Locate and identify every blood parasite.
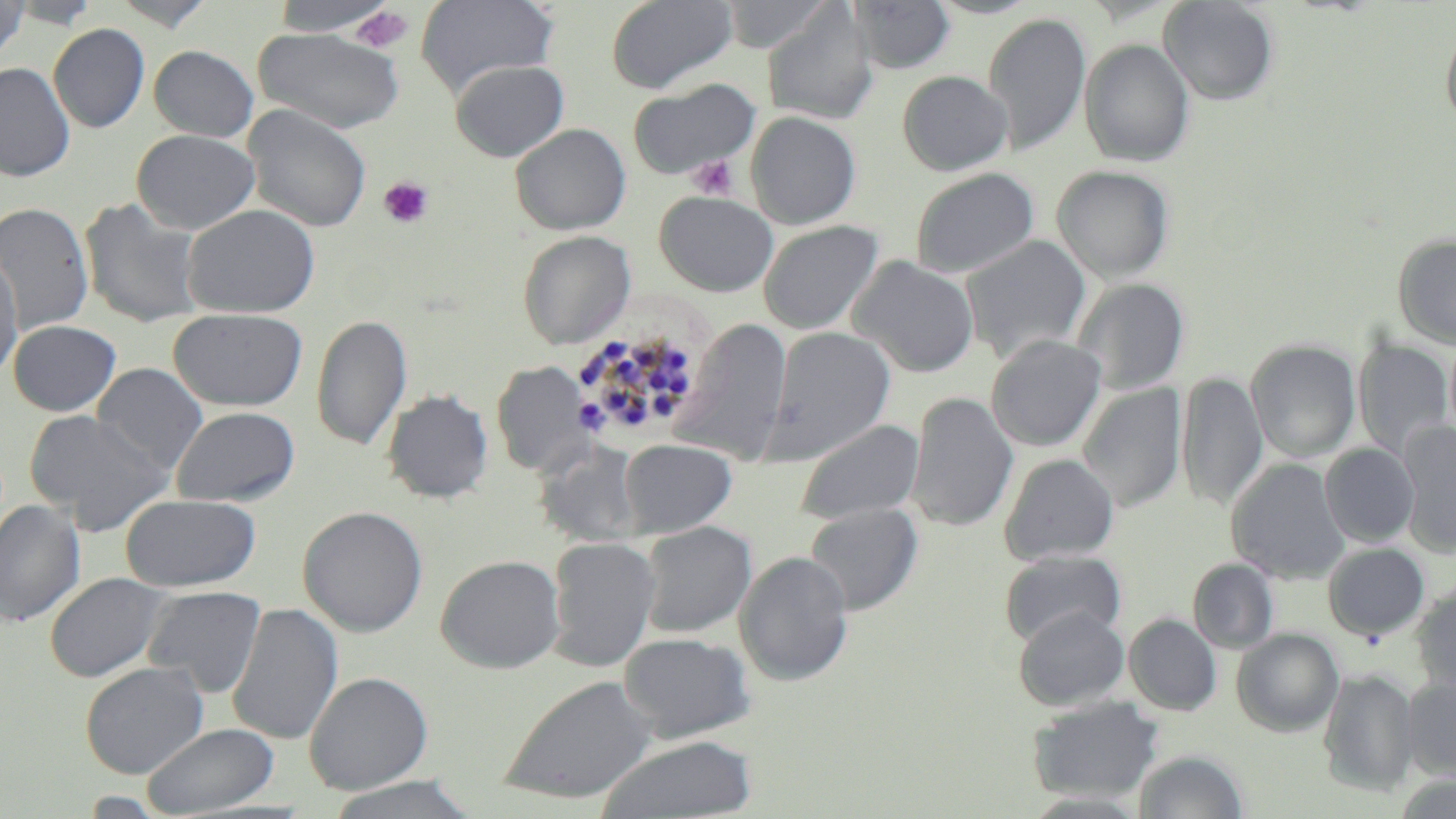
Approximate bounding boxes as named x1/y1/x2/y2 corners in pixels.
Plasmodium malariae-infected red blood cells: (x1=567, y1=328, x2=692, y2=438).
No Plasmodium falciparum, Plasmodium ovale, Plasmodium vivax, Babesia divergens, or Trypanosoma brucei observed.

Summary:
  - Uninfected red blood cell locations: (x1=0, y1=0, x2=32, y2=61), (x1=10, y1=0, x2=102, y2=29), (x1=108, y1=0, x2=216, y2=30), (x1=266, y1=0, x2=404, y2=36), (x1=415, y1=0, x2=558, y2=97), (x1=606, y1=0, x2=737, y2=94), (x1=720, y1=0, x2=834, y2=53), (x1=851, y1=0, x2=955, y2=73), (x1=927, y1=0, x2=1044, y2=19), (x1=1157, y1=0, x2=1279, y2=105), (x1=762, y1=5, x2=879, y2=125), (x1=982, y1=12, x2=1091, y2=156), (x1=48, y1=23, x2=150, y2=133), (x1=1441, y1=24, x2=1456, y2=128), (x1=252, y1=28, x2=404, y2=133), (x1=1079, y1=38, x2=1195, y2=166), (x1=148, y1=45, x2=258, y2=142), (x1=449, y1=59, x2=569, y2=162), (x1=0, y1=62, x2=75, y2=181), (x1=897, y1=70, x2=1012, y2=176), (x1=626, y1=79, x2=759, y2=180), (x1=242, y1=104, x2=372, y2=233), (x1=745, y1=111, x2=861, y2=229), (x1=510, y1=123, x2=631, y2=235), (x1=131, y1=129, x2=260, y2=235), (x1=1052, y1=165, x2=1174, y2=283), (x1=910, y1=167, x2=1039, y2=279), (x1=654, y1=191, x2=779, y2=297), (x1=79, y1=198, x2=206, y2=328), (x1=0, y1=202, x2=94, y2=335), (x1=181, y1=204, x2=320, y2=318), (x1=758, y1=220, x2=883, y2=335), (x1=518, y1=230, x2=635, y2=348), (x1=1392, y1=233, x2=1456, y2=349), (x1=960, y1=235, x2=1091, y2=363), (x1=0, y1=249, x2=24, y2=382), (x1=848, y1=256, x2=979, y2=377), (x1=1074, y1=277, x2=1189, y2=394), (x1=168, y1=307, x2=307, y2=411), (x1=312, y1=314, x2=412, y2=452), (x1=672, y1=318, x2=793, y2=464), (x1=8, y1=319, x2=121, y2=416), (x1=766, y1=325, x2=895, y2=463), (x1=985, y1=334, x2=1106, y2=452), (x1=1352, y1=338, x2=1454, y2=460), (x1=1245, y1=339, x2=1361, y2=463), (x1=492, y1=361, x2=595, y2=477), (x1=92, y1=363, x2=208, y2=476), (x1=1177, y1=372, x2=1268, y2=511), (x1=1077, y1=382, x2=1187, y2=512), (x1=382, y1=389, x2=492, y2=503), (x1=907, y1=392, x2=1018, y2=532), (x1=170, y1=406, x2=300, y2=507), (x1=23, y1=408, x2=173, y2=533), (x1=796, y1=419, x2=924, y2=525), (x1=1397, y1=421, x2=1456, y2=557), (x1=619, y1=439, x2=737, y2=538), (x1=536, y1=441, x2=646, y2=547), (x1=1320, y1=444, x2=1419, y2=546), (x1=999, y1=453, x2=1120, y2=564), (x1=1225, y1=458, x2=1350, y2=584), (x1=120, y1=493, x2=261, y2=592), (x1=0, y1=499, x2=85, y2=626), (x1=804, y1=502, x2=923, y2=616), (x1=297, y1=505, x2=428, y2=637), (x1=638, y1=520, x2=757, y2=637), (x1=546, y1=536, x2=661, y2=672), (x1=1322, y1=542, x2=1429, y2=641), (x1=999, y1=550, x2=1125, y2=648), (x1=734, y1=551, x2=854, y2=686), (x1=436, y1=554, x2=565, y2=673), (x1=1187, y1=558, x2=1278, y2=654), (x1=44, y1=572, x2=170, y2=682), (x1=1411, y1=581, x2=1456, y2=695), (x1=142, y1=585, x2=266, y2=697), (x1=226, y1=602, x2=344, y2=746), (x1=1013, y1=606, x2=1129, y2=710), (x1=1124, y1=614, x2=1222, y2=715), (x1=1231, y1=628, x2=1344, y2=736), (x1=619, y1=631, x2=755, y2=742), (x1=80, y1=662, x2=209, y2=778), (x1=1318, y1=668, x2=1420, y2=796), (x1=303, y1=671, x2=433, y2=794), (x1=499, y1=674, x2=658, y2=805), (x1=1401, y1=677, x2=1456, y2=780), (x1=1026, y1=695, x2=1164, y2=804), (x1=142, y1=722, x2=280, y2=816), (x1=595, y1=735, x2=757, y2=819), (x1=1134, y1=749, x2=1248, y2=818), (x1=324, y1=775, x2=480, y2=819)
  - Platelet locations: (x1=351, y1=6, x2=415, y2=54), (x1=685, y1=155, x2=739, y2=199), (x1=378, y1=176, x2=435, y2=230)
  - Slide-level diagnosis: Plasmodium malariae
  - Preparation: thin blood smear
  - Stain: May-Grünwald-Giemsa
  - Field of view: one of a larger specimen
  - Image size: 1456×819 pixels
  - Modality: light microscopy
  - Magnification: 1000x